Give the position of every Plasmodium parasite visible.
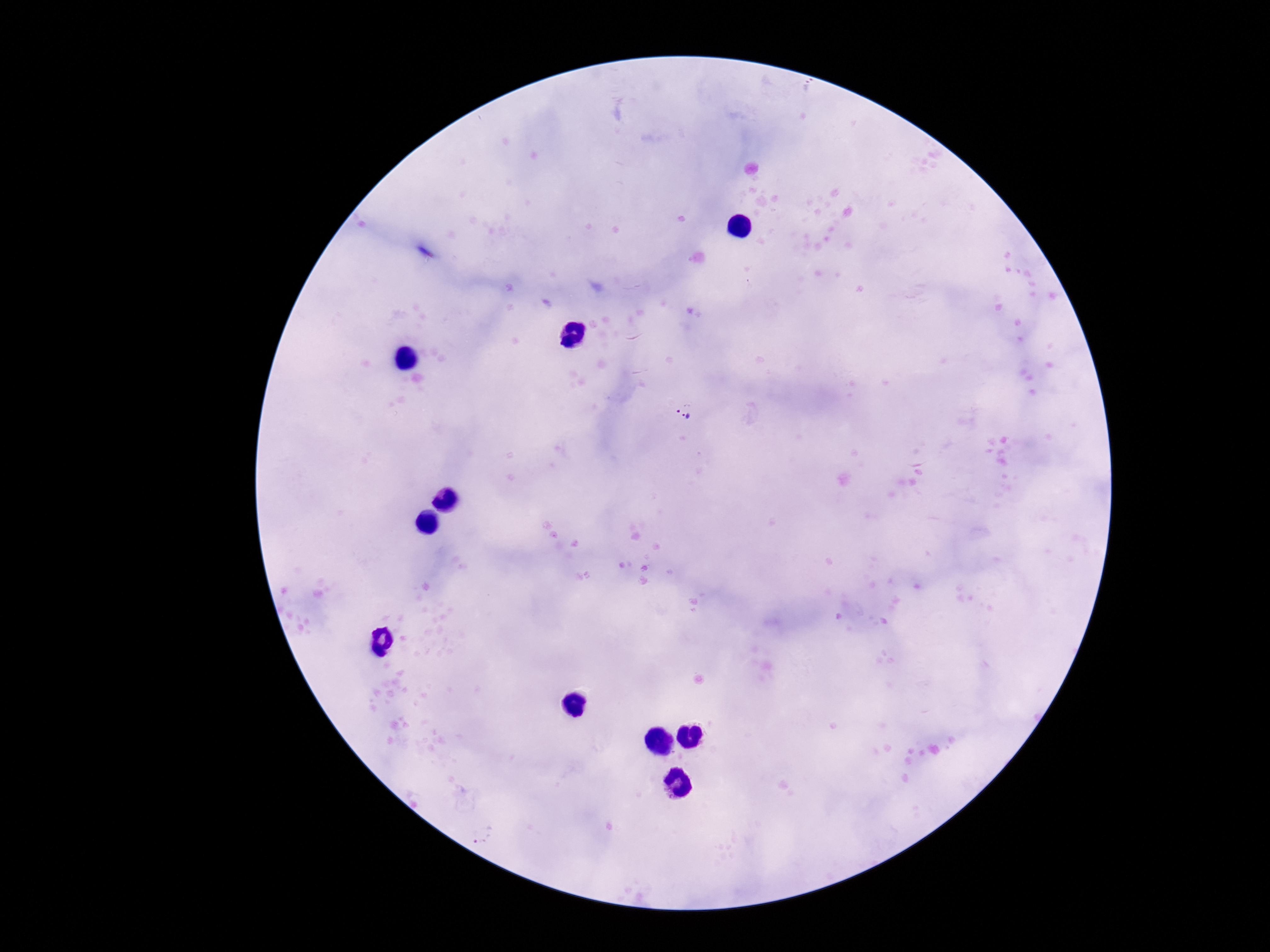
Approximate centers as (x, y) in pixels.
Plasmodium parasites: (685, 411).

Summary:
  - Preparation: thick blood film
  - Field of view: single
  - Magnification: 100x
  - Capture: smartphone camera through the microscope eyepiece
  - Patient malaria status: infected
  - Stain: Giemsa
  - Image size: 1270×952 pixels